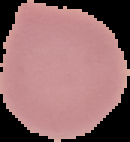
From a thin blood film. Segmented cell region on a black background. Image is 130×142 pixels. Malaria status: uninfected.